Name the blood parasite species.
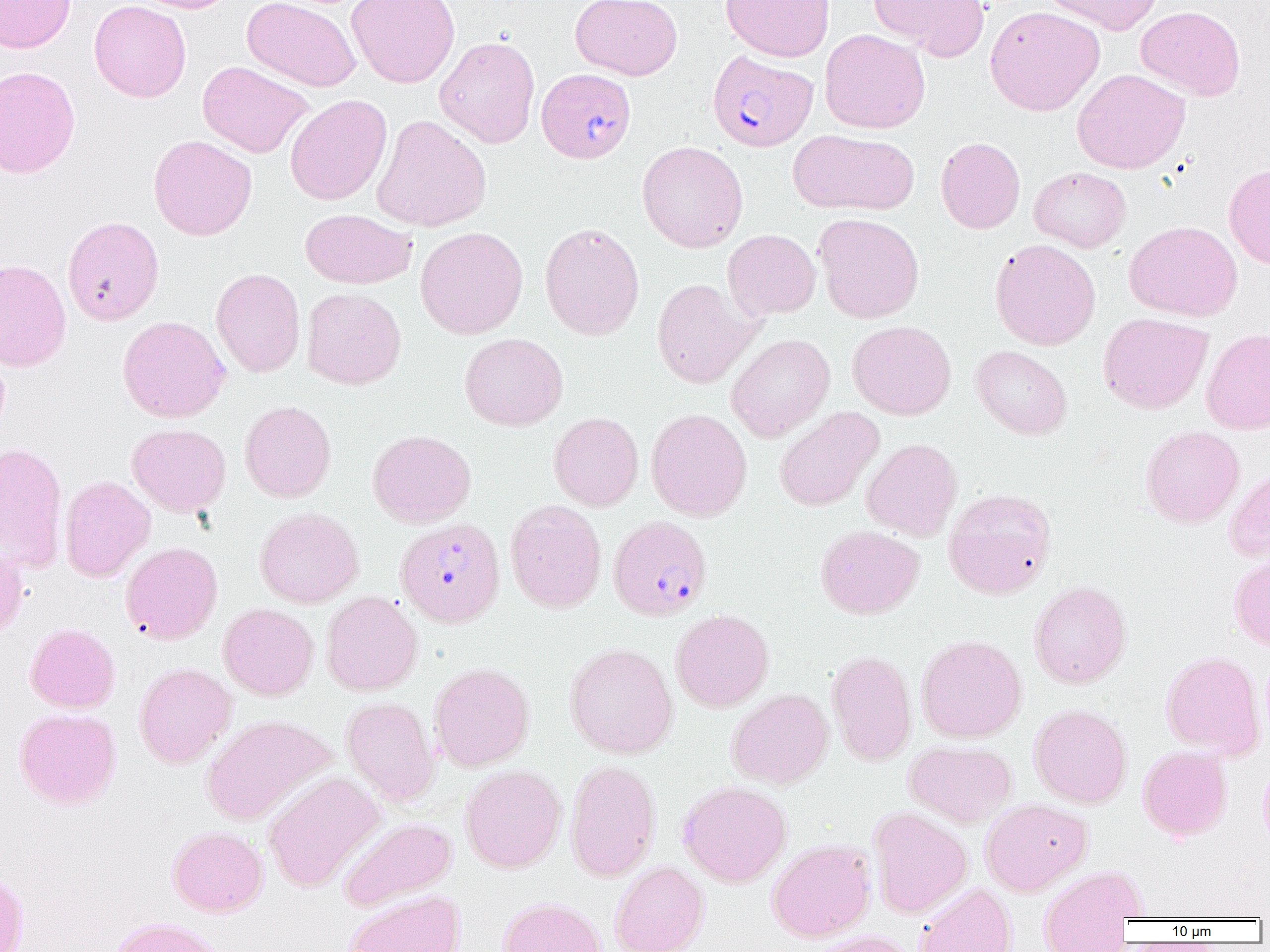
Plasmodium falciparum.

field of view = one of a larger specimen
image size = 1270×952 pixels
uninfected red blood cell locations = approximate bounding boxes as [x1, y1, x2, y2] in pixels: [0, 0, 76, 53], [89, 0, 191, 103], [129, 0, 238, 13], [242, 0, 361, 92], [346, 0, 460, 89], [570, 0, 682, 80], [720, 0, 835, 62], [869, 0, 989, 60], [1040, 0, 1163, 35], [1135, 5, 1246, 101], [985, 6, 1104, 116], [819, 28, 930, 134], [434, 35, 540, 148], [197, 61, 314, 158], [0, 65, 80, 178], [1072, 68, 1190, 174], [285, 94, 392, 205], [371, 115, 491, 232], [788, 129, 919, 216], [148, 135, 257, 241], [936, 137, 1025, 234], [637, 141, 748, 252], [1224, 162, 1270, 269], [1029, 167, 1131, 253], [300, 208, 417, 289], [814, 213, 925, 324], [62, 216, 164, 326], [1124, 220, 1242, 321], [539, 222, 645, 340], [415, 226, 528, 339], [722, 229, 820, 320], [989, 238, 1101, 350], [0, 259, 72, 372], [211, 268, 306, 378], [652, 278, 760, 388], [301, 287, 406, 389], [1098, 313, 1212, 414], [117, 316, 230, 423], [847, 320, 956, 420], [1201, 328, 1270, 435], [459, 333, 568, 431], [726, 334, 835, 442], [971, 345, 1072, 440], [239, 400, 336, 502], [774, 407, 884, 512], [646, 408, 752, 521], [549, 412, 644, 511], [127, 424, 231, 516], [1140, 425, 1244, 527], [367, 429, 476, 527], [862, 438, 962, 541], [0, 442, 68, 571], [1223, 467, 1270, 563], [59, 475, 154, 582], [943, 488, 1057, 599], [505, 499, 606, 613], [255, 507, 363, 608], [815, 525, 924, 619], [0, 539, 28, 641], [120, 541, 223, 644], [1228, 554, 1270, 652], [1029, 581, 1131, 688], [321, 591, 423, 696], [218, 603, 319, 700], [671, 609, 774, 712], [24, 623, 120, 713], [916, 634, 1026, 742], [564, 643, 677, 759], [826, 650, 917, 766], [1161, 650, 1264, 759], [134, 662, 236, 768], [429, 662, 534, 772], [726, 689, 833, 789], [341, 696, 440, 806], [1029, 704, 1132, 808], [14, 708, 121, 810], [201, 714, 335, 826], [904, 740, 1017, 828], [1137, 745, 1232, 841], [1259, 758, 1270, 854], [565, 760, 661, 881], [460, 764, 566, 873], [262, 771, 385, 892], [678, 780, 791, 887], [980, 798, 1092, 896], [868, 806, 972, 918], [339, 816, 457, 911], [167, 826, 268, 917], [767, 839, 876, 942], [609, 862, 708, 952], [0, 866, 29, 951], [1038, 866, 1146, 951], [914, 884, 1016, 952], [344, 889, 465, 952], [498, 897, 605, 952], [109, 917, 226, 952], [802, 930, 919, 952]
magnification = 1000x
preparation = thin blood smear
Plasmodium falciparum-infected red blood cell locations = approximate bounding boxes as [x1, y1, x2, y2] in pixels: [707, 50, 818, 152], [536, 67, 636, 163], [609, 516, 711, 620], [396, 517, 505, 627]
modality = optical microscopy